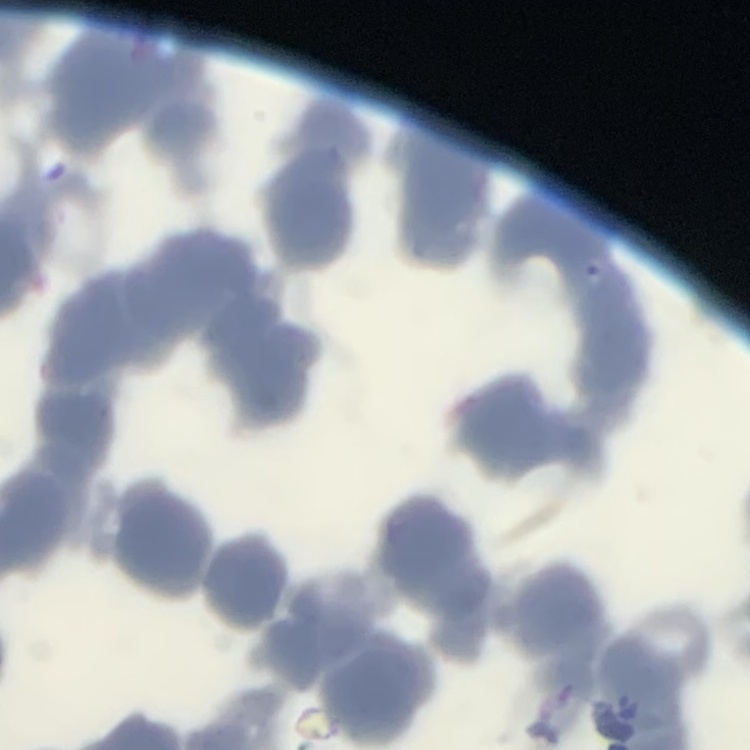 The red blood cells exhibit rouleaux formation. Square crop of a larger photomicrograph. Thin blood smear. Field's or Giemsa stain.